Find each parasitized red blood cell.
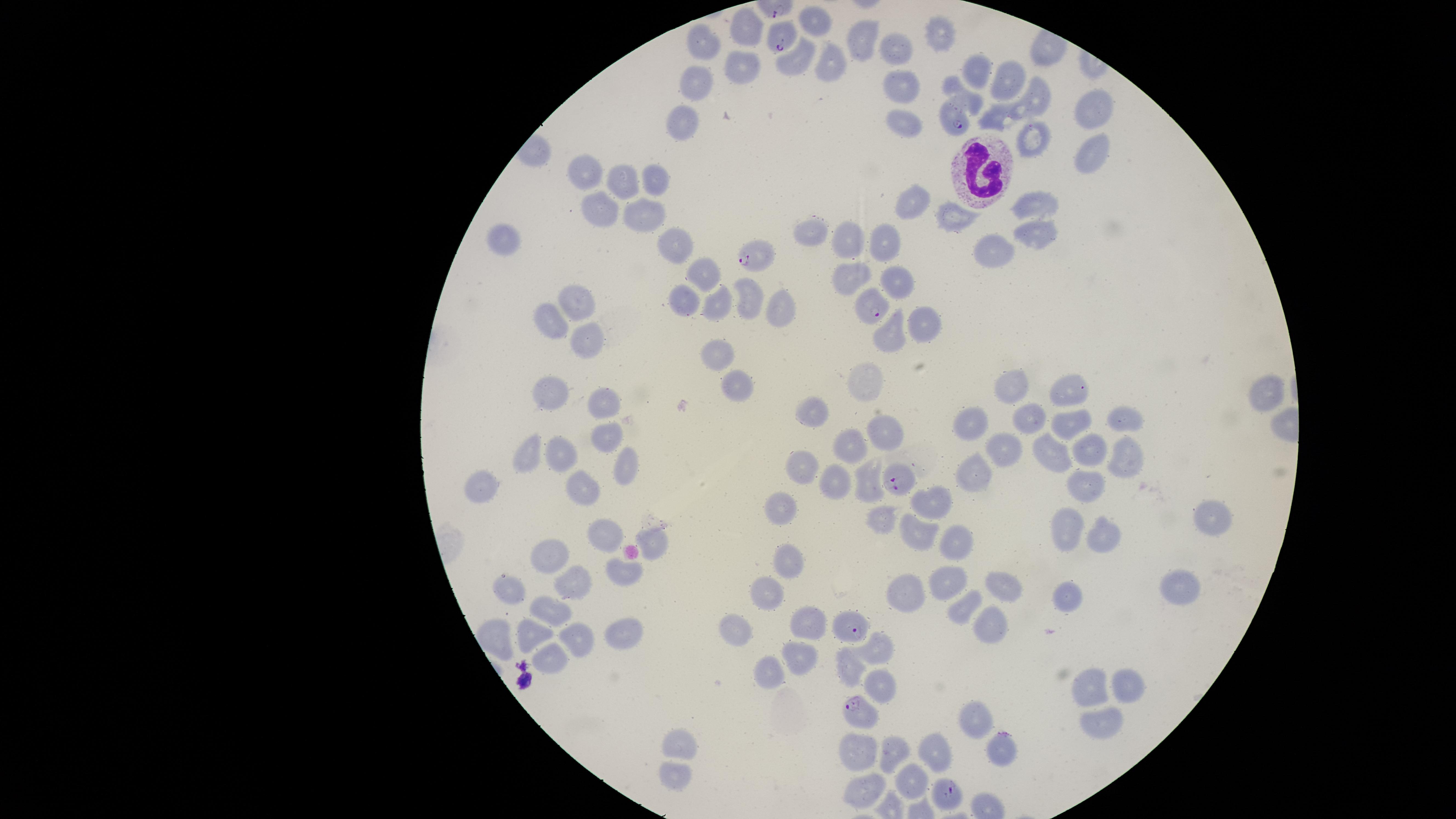

Approximate marker points as (x, y) in pixels.
Parasitized red blood cells: (782, 34), (956, 119), (758, 260), (870, 311), (894, 482), (846, 631), (855, 707), (1002, 747), (944, 793).

capture = smartphone photograph through the microscope eyepiece
stain = Giemsa
image size = 1456×819 pixels
preparation = thin blood smear
white blood cells = approximate marker points as (x, y) in pixels: (973, 168)
field of view = single
visible region = circular
species = Plasmodium falciparum
uninfected red blood cells = approximate marker points as (x, y) in pixels: (747, 30), (938, 33), (863, 36), (706, 43), (896, 55), (797, 62), (832, 65), (737, 67), (699, 78), (1008, 80), (905, 88), (1038, 100), (1089, 112), (902, 117), (1004, 117), (684, 119), (1035, 136), (1098, 155), (588, 173), (657, 179), (623, 181), (916, 201), (1042, 205), (599, 210), (643, 215), (961, 220), (813, 233), (1038, 234), (508, 241), (850, 241), (679, 243), (890, 243), (992, 251), (848, 270), (701, 273), (896, 278), (746, 297), (576, 302), (689, 302), (721, 305), (773, 306), (924, 318), (555, 326), (890, 333), (592, 340), (721, 354), (876, 381), (740, 390), (1014, 391), (1069, 391), (560, 395), (1261, 395), (611, 402), (1033, 417), (1126, 417), (819, 418), (981, 421), (1075, 423), (611, 435), (888, 435), (854, 444), (1002, 449), (1087, 449), (538, 453), (1056, 453), (566, 454), (1126, 457), (623, 468), (804, 470), (976, 475), (490, 484), (832, 485), (586, 491), (1086, 492), (938, 500), (784, 506), (1206, 517), (917, 526), (1067, 528), (1103, 537), (609, 539), (957, 540), (552, 556), (791, 562), (954, 580), (574, 583), (1002, 585), (511, 586), (1176, 586), (915, 591), (774, 594), (1069, 596), (967, 604), (554, 609), (804, 622), (984, 627), (621, 628), (738, 631), (500, 634), (532, 635), (577, 637), (878, 647), (796, 655), (558, 658), (852, 661), (772, 667), (1089, 684), (1129, 685), (880, 690), (976, 721), (1102, 722), (682, 741), (861, 746), (896, 749), (934, 751), (670, 772), (909, 777), (865, 786)